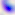
Summary:
  - Magnification: 400x
  - Modality: photomicrograph
  - Identification: Toxoplasma gondii